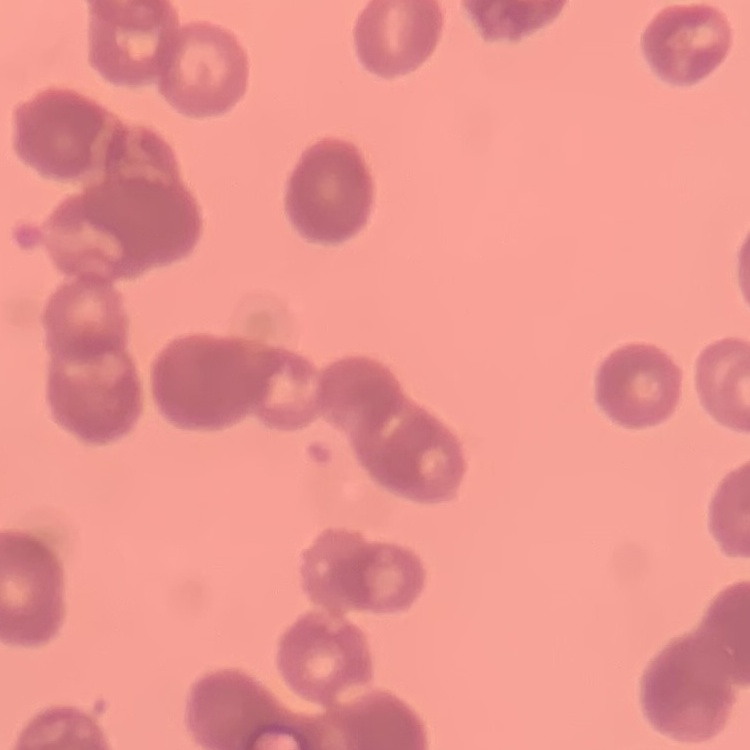
The red blood cells exhibit rouleaux formation. Stained with either Field's or Giemsa. Thin blood smear. Square crop of a larger photomicrograph.